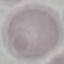

Malaria status: uninfected. Giemsa-stained preparation. Photographed with a smartphone camera at the microscope eyepiece. Thin blood film. Cell patch, automatically extracted from a larger field of view and resized to 64 × 64 pixels.